Assess the morphology of the red blood cells.
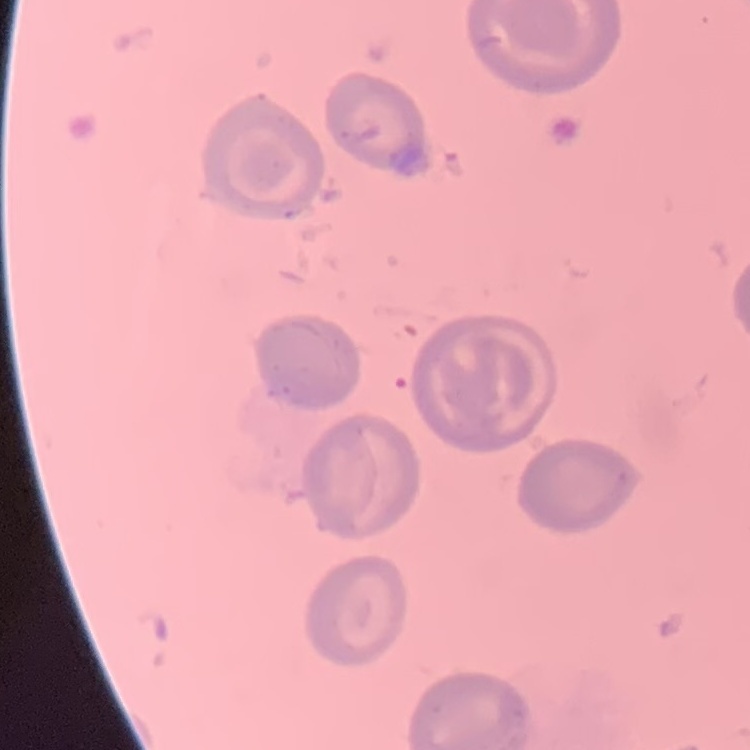
No rouleaux formation.

Summary:
  - Stain: Field's or Giemsa
  - Preparation: thin blood film
  - Image type: one tile cut from a larger photomicrograph